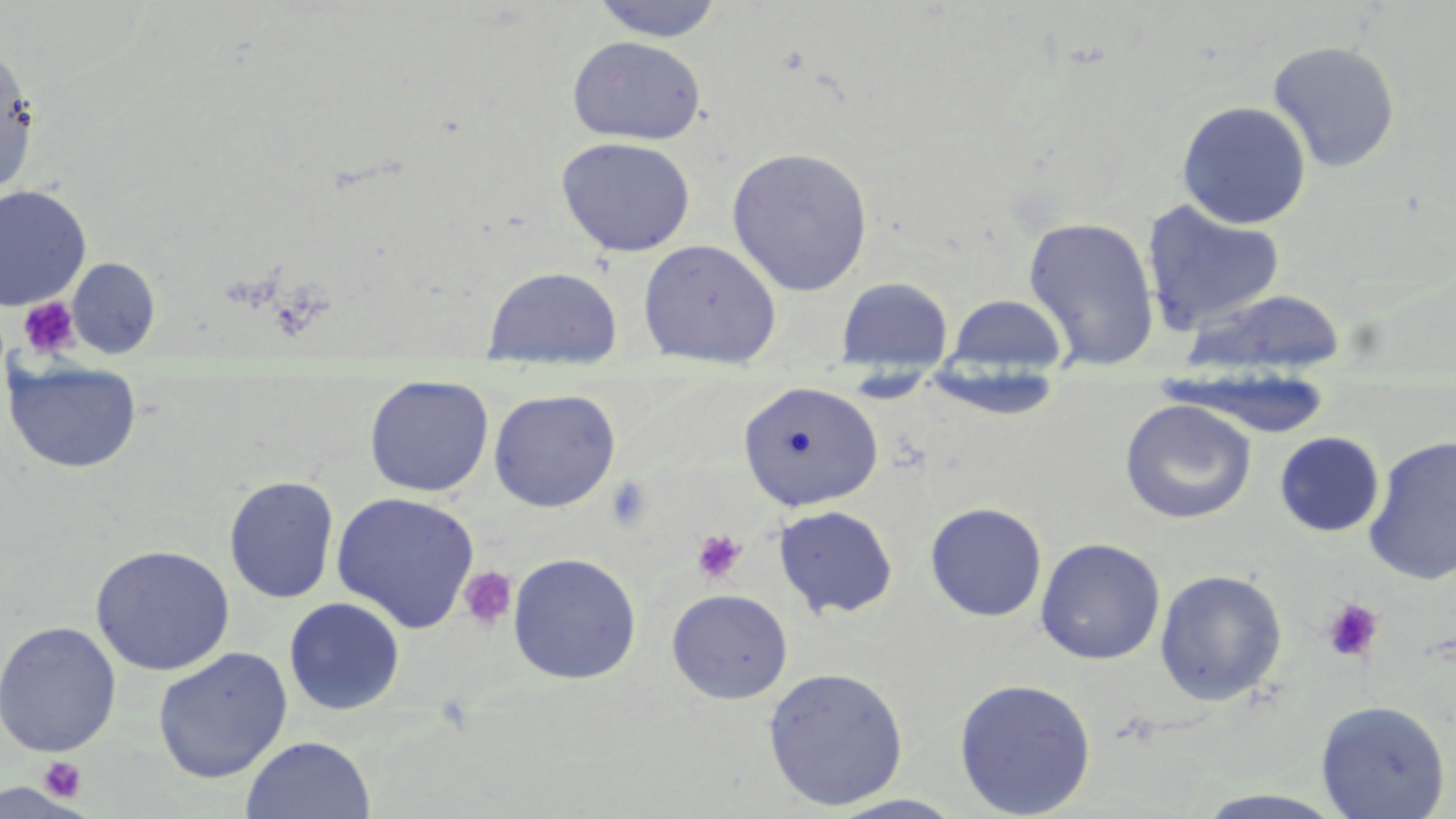
{
  "slide_level_diagnosis": "no evidence of blood parasites",
  "image_size": "1456×819 pixels",
  "modality": "light microscopy",
  "preparation": "thin blood film",
  "uninfected_red_blood_cell_locations": "approximate bounding boxes as (x1,y1)-(x2,y2) corner pairs in pixels: (588,0)-(727,43), (567,35)-(708,145), (1267,40)-(1401,173), (0,45)-(39,197), (1177,100)-(1312,229), (555,136)-(697,257), (727,147)-(874,296), (0,185)-(92,311), (1141,199)-(1287,336), (1022,215)-(1161,371), (638,239)-(782,361), (67,257)-(161,358), (482,266)-(623,361), (837,276)-(953,374), (1181,288)-(1346,378), (946,293)-(1069,378), (4,359)-(143,474), (1162,368)-(1334,440), (364,374)-(494,497), (738,381)-(883,511), (488,388)-(621,512), (1119,398)-(1257,524), (1274,432)-(1384,537), (1363,435)-(1456,585), (223,475)-(340,604), (331,490)-(481,633), (925,502)-(1048,622), (773,505)-(899,618), (1035,537)-(1165,665), (90,544)-(235,676), (507,552)-(642,685), (1154,569)-(1287,705), (666,588)-(793,704), (283,597)-(406,716), (0,620)-(122,757), (152,647)-(292,783), (763,666)-(909,811), (953,677)-(1097,818), (1315,699)-(1452,818), (240,735)-(376,819), (1189,790)-(1353,819), (826,794)-(970,817)",
  "platelet_locations": "approximate bounding boxes as (x1,y1)-(x2,y2) corner pairs in pixels: (17,297)-(82,360), (605,476)-(654,529), (692,529)-(747,584), (458,567)-(517,631), (1321,597)-(1384,663), (38,756)-(88,804)",
  "stain": "May-Grünwald-Giemsa",
  "magnification": "1000x",
  "field_of_view": "single"
}